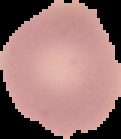
preparation = thin blood smear
image size = 121×139 pixels
image type = cell region segmented out of the field of view; surrounding area masked to black
result = no malaria parasites detected